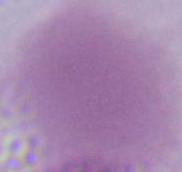
{
  "magnification": "1000x",
  "modality": "photomicrograph",
  "identification": "erythrocyte"
}